Identify the parasite.
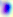
Toxoplasma gondii.

Summary:
  - Modality: photomicrograph
  - Magnification: 400x